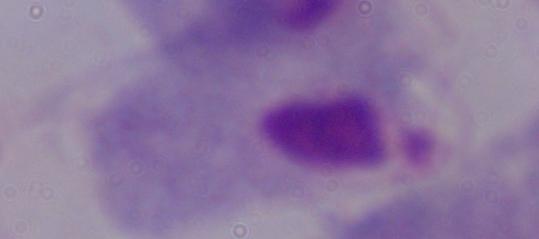
Summary:
  - Modality: photomicrograph
  - Identification: trichomonad
  - Magnification: 1000x